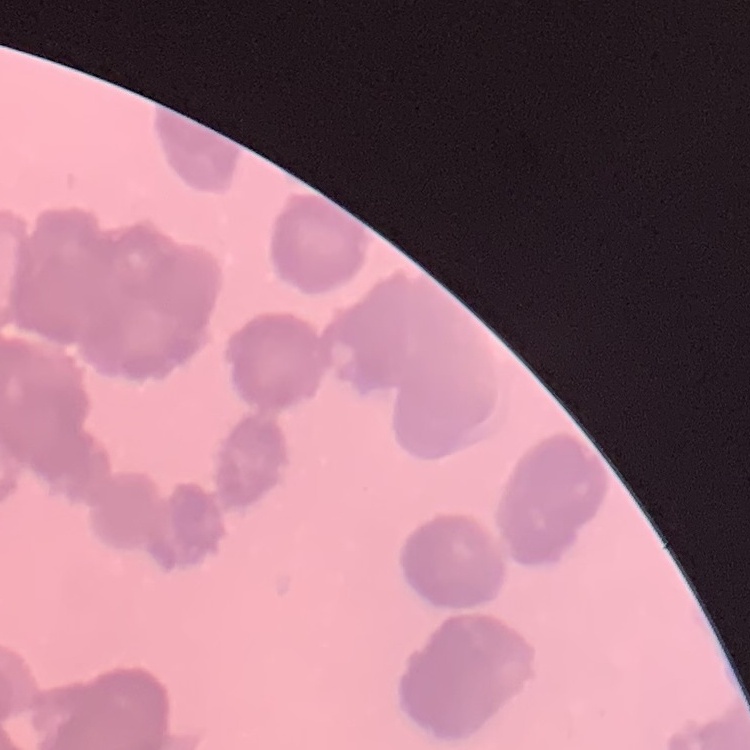
The red blood cells show rouleaux formation. Square crop of a larger photomicrograph. Stained with either Field's or Giemsa. Thin peripheral smear.